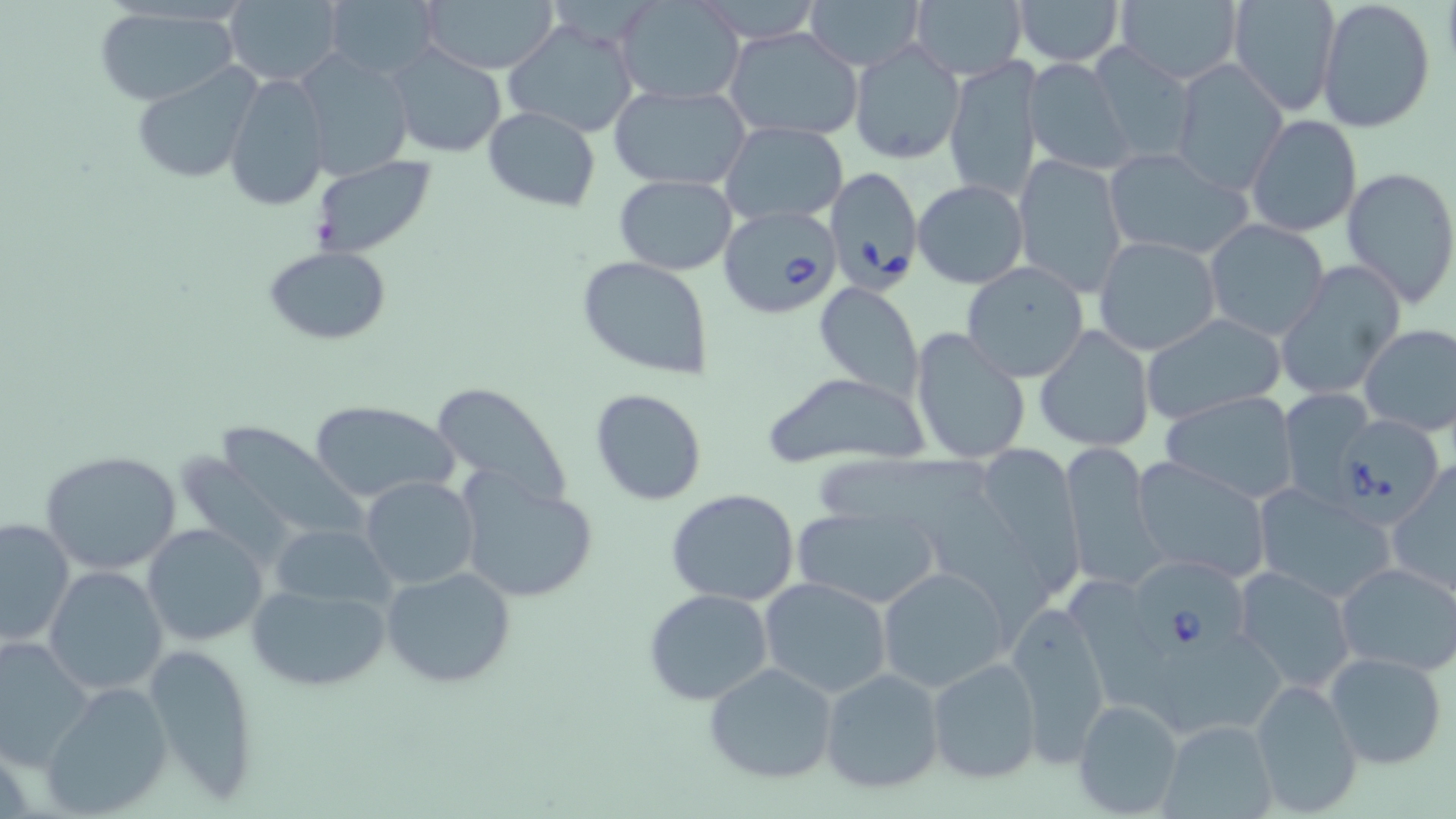

slide-level diagnosis = Babesia divergens
field of view = single
preparation = thin blood film
modality = optical microscopy
stain = May-Grünwald-Giemsa
magnification = 1000x
Babesia divergens-infected red blood cell locations = approximate bounding boxes as named x1/y1/x2/y2 corners in pixels: (x1=826, y1=168, x2=925, y2=288), (x1=716, y1=204, x2=844, y2=319), (x1=1336, y1=415, x2=1444, y2=534), (x1=1125, y1=560, x2=1247, y2=662)
uninfected red blood cell locations = approximate bounding boxes as named x1/y1/x2/y2 corners in pixels: (x1=222, y1=0, x2=345, y2=87), (x1=321, y1=0, x2=440, y2=79), (x1=420, y1=0, x2=561, y2=74), (x1=615, y1=0, x2=747, y2=106), (x1=807, y1=0, x2=923, y2=68), (x1=1013, y1=0, x2=1123, y2=66), (x1=1229, y1=0, x2=1338, y2=115), (x1=1317, y1=1, x2=1436, y2=135), (x1=907, y1=2, x2=1027, y2=82), (x1=1116, y1=2, x2=1241, y2=85), (x1=94, y1=6, x2=241, y2=107), (x1=503, y1=17, x2=641, y2=140), (x1=721, y1=26, x2=865, y2=143), (x1=849, y1=40, x2=965, y2=165), (x1=388, y1=43, x2=506, y2=157), (x1=1087, y1=43, x2=1196, y2=168), (x1=297, y1=49, x2=415, y2=182), (x1=943, y1=57, x2=1043, y2=201), (x1=1022, y1=58, x2=1133, y2=176), (x1=1171, y1=60, x2=1287, y2=195), (x1=131, y1=63, x2=260, y2=185), (x1=224, y1=72, x2=332, y2=212), (x1=607, y1=83, x2=752, y2=190), (x1=482, y1=107, x2=602, y2=211), (x1=1247, y1=115, x2=1362, y2=238), (x1=721, y1=121, x2=849, y2=226), (x1=1105, y1=149, x2=1250, y2=263), (x1=1012, y1=154, x2=1128, y2=296), (x1=309, y1=156, x2=438, y2=256), (x1=1339, y1=166, x2=1456, y2=306), (x1=613, y1=175, x2=737, y2=275), (x1=912, y1=179, x2=1029, y2=289), (x1=1204, y1=219, x2=1330, y2=339), (x1=1093, y1=236, x2=1223, y2=356), (x1=265, y1=246, x2=391, y2=344), (x1=577, y1=256, x2=713, y2=381), (x1=961, y1=261, x2=1090, y2=382), (x1=1276, y1=262, x2=1405, y2=401), (x1=814, y1=283, x2=923, y2=399), (x1=1139, y1=312, x2=1286, y2=425), (x1=1358, y1=322, x2=1456, y2=439), (x1=1034, y1=325, x2=1155, y2=453), (x1=910, y1=327, x2=1034, y2=465), (x1=761, y1=372, x2=932, y2=472), (x1=428, y1=381, x2=574, y2=508), (x1=589, y1=387, x2=708, y2=508), (x1=1281, y1=387, x2=1373, y2=505), (x1=1160, y1=393, x2=1300, y2=501), (x1=310, y1=399, x2=459, y2=504), (x1=205, y1=424, x2=370, y2=544), (x1=1062, y1=441, x2=1159, y2=591), (x1=960, y1=445, x2=1088, y2=593), (x1=38, y1=450, x2=186, y2=577), (x1=817, y1=453, x2=997, y2=523), (x1=1129, y1=454, x2=1270, y2=579), (x1=1388, y1=463, x2=1455, y2=600), (x1=457, y1=474, x2=600, y2=605), (x1=359, y1=476, x2=479, y2=591), (x1=921, y1=485, x2=1055, y2=648), (x1=665, y1=488, x2=801, y2=606), (x1=1255, y1=488, x2=1397, y2=604), (x1=788, y1=506, x2=941, y2=609), (x1=1, y1=517, x2=75, y2=649), (x1=143, y1=523, x2=269, y2=647), (x1=268, y1=523, x2=395, y2=610), (x1=1335, y1=562, x2=1456, y2=674), (x1=1231, y1=565, x2=1355, y2=694), (x1=44, y1=566, x2=169, y2=696), (x1=380, y1=566, x2=518, y2=689), (x1=878, y1=566, x2=1009, y2=694), (x1=759, y1=578, x2=893, y2=699), (x1=1071, y1=578, x2=1180, y2=722), (x1=245, y1=582, x2=390, y2=692), (x1=643, y1=588, x2=775, y2=706), (x1=19, y1=595, x2=136, y2=749), (x1=1005, y1=599, x2=1113, y2=762), (x1=0, y1=634, x2=95, y2=770), (x1=1140, y1=639, x2=1289, y2=735), (x1=143, y1=641, x2=263, y2=804), (x1=1325, y1=652, x2=1449, y2=771), (x1=925, y1=656, x2=1044, y2=784), (x1=703, y1=662, x2=839, y2=785), (x1=819, y1=667, x2=945, y2=794), (x1=1249, y1=677, x2=1360, y2=815), (x1=40, y1=682, x2=174, y2=817), (x1=1071, y1=699, x2=1184, y2=815), (x1=1160, y1=719, x2=1278, y2=819)
image size = 1456×819 pixels